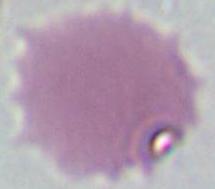

An erythrocyte is seen. Captured at 1000x magnification. Micrograph.